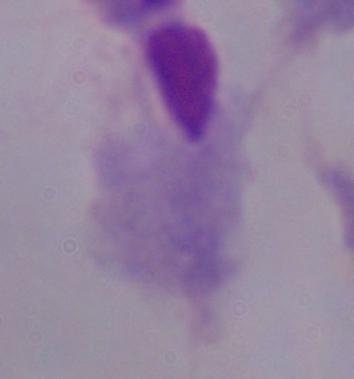
Summary:
  - Modality: micrograph
  - Magnification: 1000x
  - Identification: trichomonad